Assess the morphology of the erythrocytes.
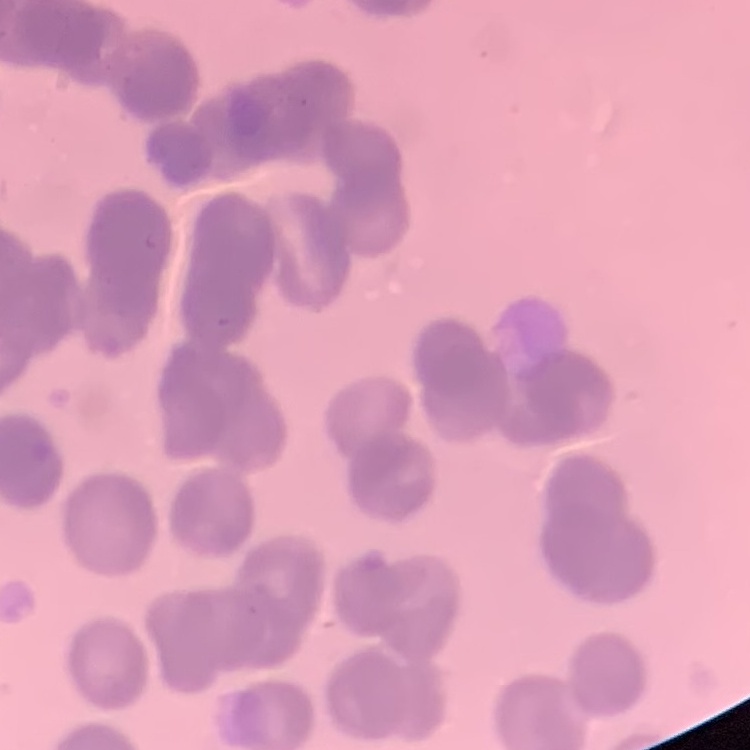
Rouleaux formation.

preparation = thin blood film
image type = square crop of a larger photomicrograph
stain = Field's or Giemsa